Assess this cell for malaria.
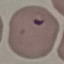

Parasitized.

Cell patch, automatically extracted from a larger field of view and resized to 64 × 64 pixels. Acquired by smartphone through the microscope eyepiece. Giemsa stain. Thin blood film.